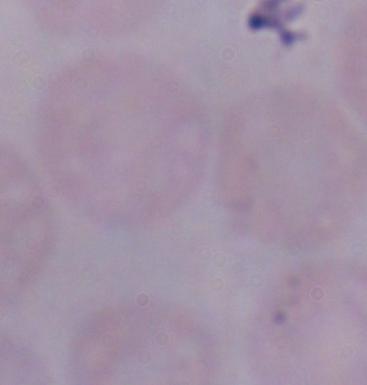

Summary:
  - Modality: micrograph
  - Magnification: 1000x
  - Identification: trypanosome